Identify the parasite.
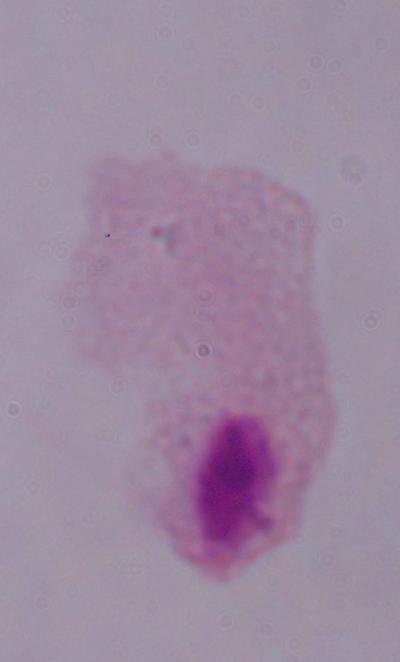
This is a trichomonad.

Captured at 1000x magnification. Micrograph.